State the blood parasite species.
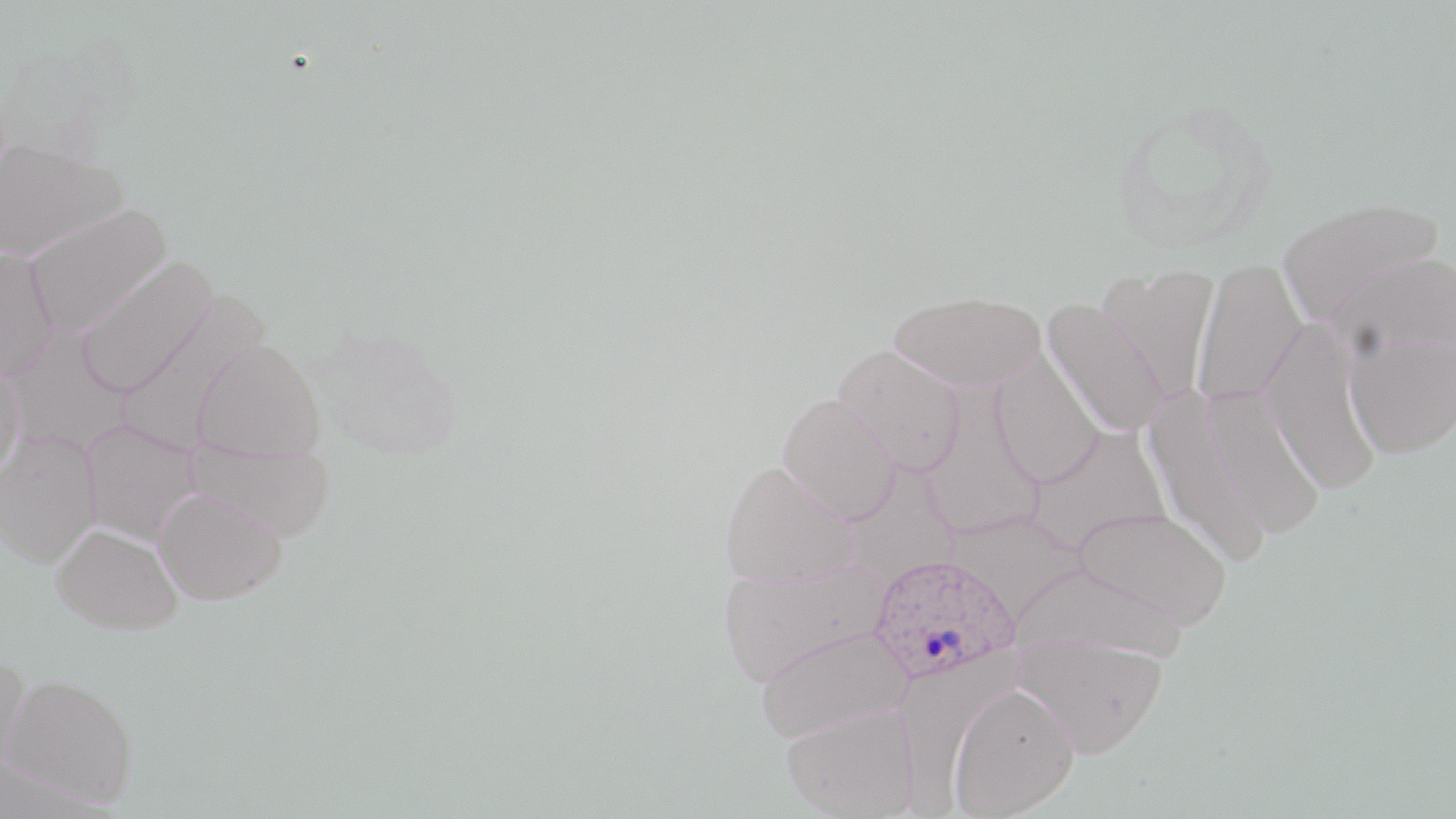
Plasmodium ovale.

stain: May-Grünwald-Giemsa
preparation: thin blood smear
field_of_view: single
uninfected_red_blood_cell_locations: 'approximate bounding boxes as [x1, y1, x2, y2] in pixels: [0, 138, 127, 261], [1274, 195, 1446, 332], [22, 202, 173, 337], [0, 247, 58, 380], [76, 257, 217, 397], [1192, 257, 1308, 409], [1097, 264, 1219, 406], [888, 289, 1047, 391], [117, 293, 269, 453], [1041, 298, 1169, 436], [1260, 320, 1383, 496], [5, 329, 132, 457], [1345, 333, 1456, 460], [192, 338, 326, 462], [834, 344, 967, 476], [990, 351, 1105, 486], [0, 358, 25, 483], [1200, 384, 1327, 540], [1139, 385, 1277, 568], [919, 389, 1044, 540], [778, 393, 900, 524], [81, 419, 202, 544], [1026, 425, 1172, 556], [0, 429, 101, 567], [186, 440, 336, 542], [719, 460, 859, 588], [841, 462, 961, 589], [153, 487, 287, 605], [1072, 507, 1232, 631], [51, 523, 182, 634], [719, 558, 890, 686], [1010, 561, 1190, 666], [754, 625, 911, 743], [1011, 631, 1168, 757], [0, 653, 32, 781], [1, 672, 138, 806], [946, 681, 1080, 817], [782, 702, 918, 818]'
magnification: 1000x
plasmodium_ovale_infected_red_blood_cell_locations: 'approximate bounding boxes as [x1, y1, x2, y2] in pixels: [870, 554, 1019, 685]'
image_size: 1456×819 pixels
modality: optical microscopy